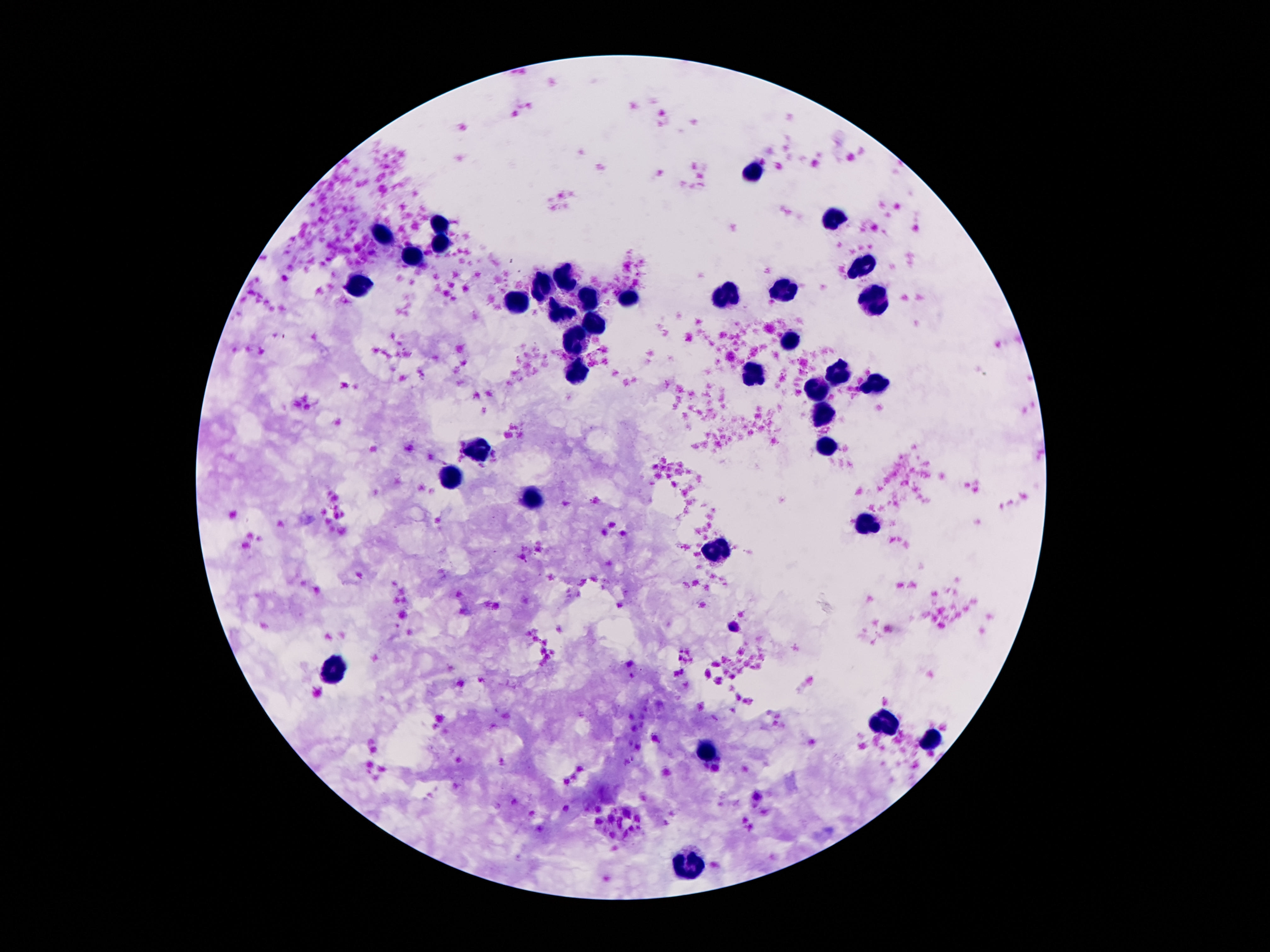 Approximate centers as [x, y] in pixels. Leukocyte locations: [751, 170], [837, 222], [443, 224], [382, 236], [442, 241], [410, 257], [863, 269], [565, 279], [547, 287], [786, 288], [362, 291], [727, 294], [626, 299], [517, 300], [875, 300], [588, 301], [562, 313], [593, 322], [575, 338], [787, 343], [750, 373], [578, 376], [840, 376], [872, 384], [819, 392], [822, 415], [478, 443], [825, 450], [450, 480], [535, 499], [868, 521], [717, 549], [334, 667], [886, 722], [934, 743], [707, 750], [690, 861]. Photographed through the microscope eyepiece with a smartphone camera. Image is 1270×952 pixels. Thick blood film. Patient malaria status: negative. Single field of view. 100x magnification. Giemsa-stained preparation.